State which cell type is depicted.
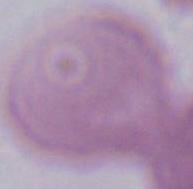
This is an erythrocyte.

modality = micrograph
magnification = 1000x